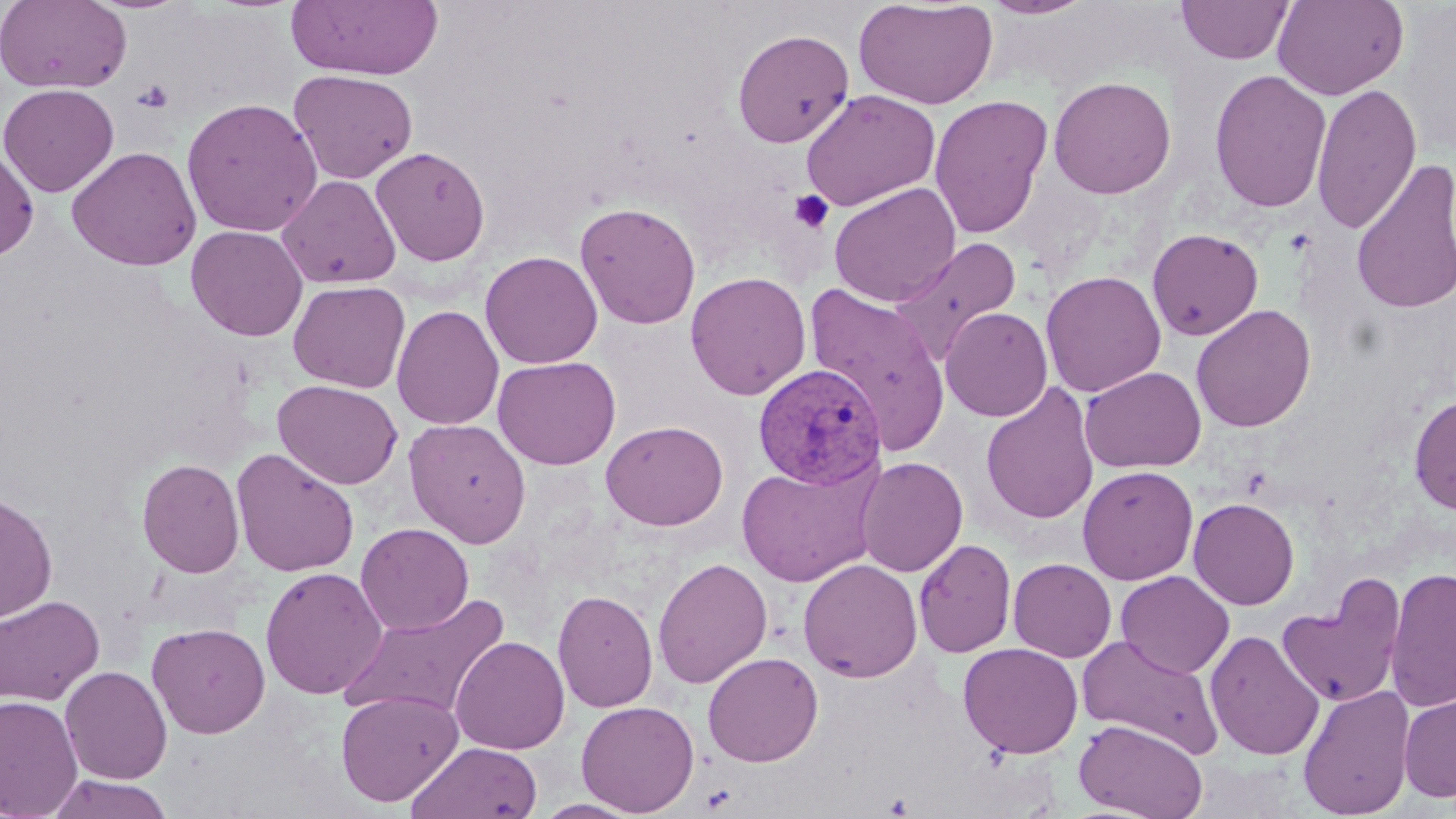
Approximate bounding boxes as (x1,y1)-(x2,y2) corner pairs in pixels. Uninfected red blood cell locations: (0,0)-(132,94), (854,0)-(998,110), (981,0)-(1099,20), (1176,0)-(1294,64), (1272,0)-(1409,100), (285,1)-(443,81), (732,27)-(855,148), (288,68)-(419,185), (1209,68)-(1331,213), (1048,76)-(1177,199), (1311,82)-(1423,234), (0,83)-(120,197), (801,89)-(940,211), (928,95)-(1053,239), (181,97)-(323,237), (0,145)-(39,262), (66,146)-(202,271), (370,146)-(491,267), (1350,158)-(1456,316), (276,174)-(402,289), (828,183)-(961,307), (574,202)-(701,329), (185,225)-(308,341), (1146,227)-(1264,341), (889,237)-(1021,367), (479,251)-(603,369), (1041,270)-(1166,397), (685,271)-(812,400), (288,280)-(410,393), (805,283)-(951,456), (392,304)-(505,430), (1191,304)-(1316,432), (940,307)-(1053,422), (492,355)-(621,469), (1080,366)-(1206,473), (272,379)-(403,490), (980,382)-(1100,526), (1408,393)-(1456,516), (403,418)-(532,548), (601,420)-(728,530), (230,448)-(360,578), (856,456)-(968,577), (137,458)-(245,578), (735,461)-(880,587), (1078,465)-(1198,585), (0,491)-(58,624), (1188,497)-(1299,609), (356,523)-(474,634), (914,539)-(1016,658), (652,557)-(773,689), (798,558)-(923,683), (1007,558)-(1117,662), (260,566)-(387,700), (1385,566)-(1456,712), (1116,570)-(1235,679), (1276,574)-(1407,709), (553,589)-(658,712), (338,592)-(511,723), (0,594)-(105,706), (147,622)-(270,739), (1204,629)-(1325,760), (1076,632)-(1225,760), (450,636)-(570,754), (958,642)-(1083,758), (702,651)-(823,767), (59,664)-(173,784), (1298,684)-(1416,818), (336,689)-(463,806), (1399,691)-(1456,803), (0,695)-(83,819), (576,700)-(699,816), (1074,719)-(1208,819), (407,741)-(543,819), (45,774)-(176,819), (532,798)-(645,818). Plasmodium vivax-infected red blood cell locations: (752,360)-(890,488). Platelet locations: (132,79)-(174,113), (788,189)-(834,234). Slide-level diagnosis: Plasmodium vivax. Image is 1456×819 pixels. May-Grünwald-Giemsa stain. Light microscopy. Captured at 1000x magnification. Single field of view. Thin blood smear.